Draw a bounding box around every parasitised red blood cell, every trophozoite, every gametocyte, every leukocyte, and every artifact (platelet-like body, stain precipitate, or debris).
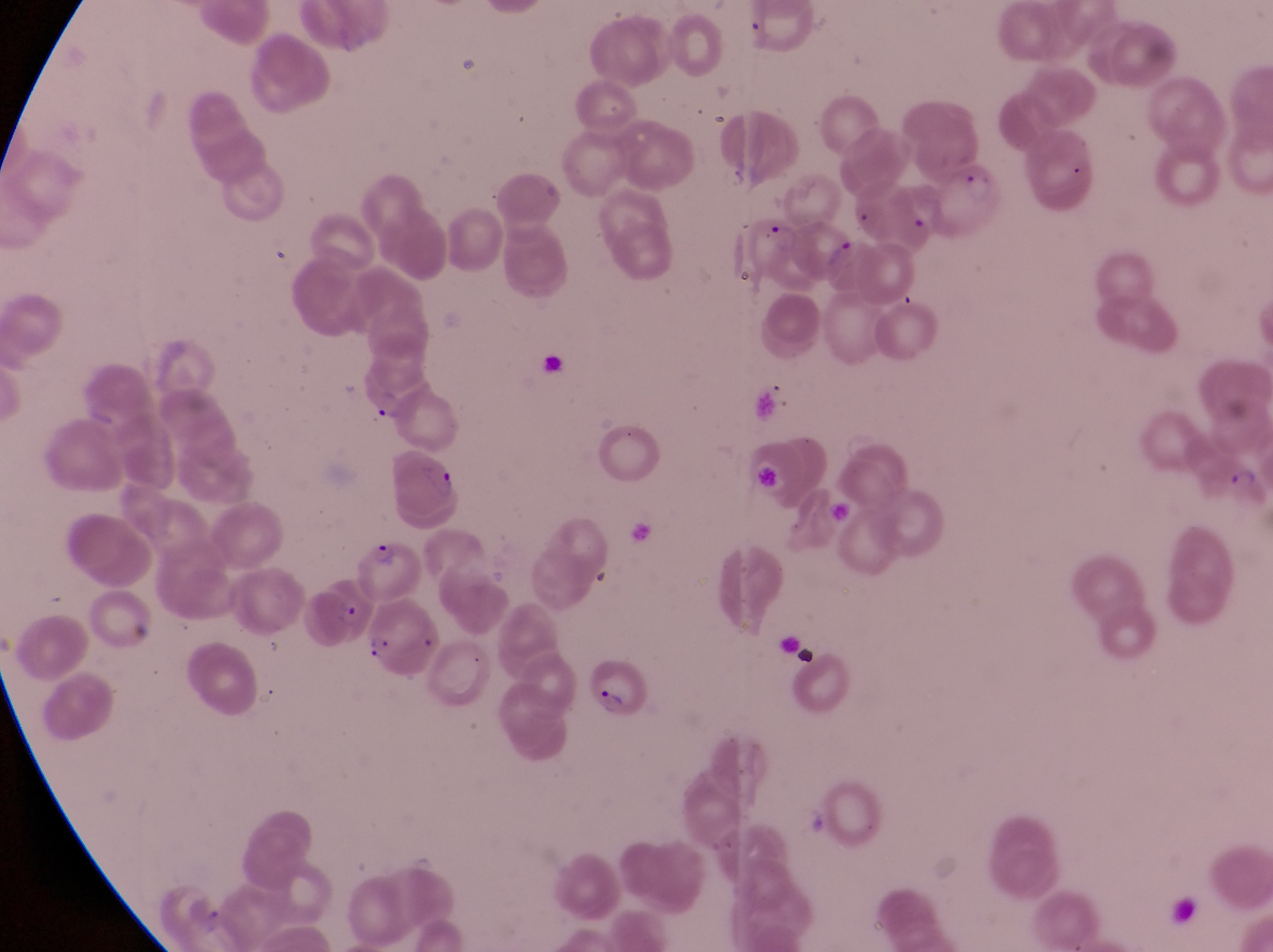
Approximate bounding boxes as {left, top, right, bottom} in pixels.
Parasitised red blood cells: {938, 164, 1010, 236}, {734, 212, 808, 295}, {819, 234, 886, 302}, {391, 457, 469, 532}, {352, 537, 427, 594}, {315, 579, 384, 641}, {581, 652, 661, 724}.
No leukocytes observed.
Artifacts (platelet-like body, stain precipitate, or debris): {776, 635, 818, 667}.

capture = smartphone photograph through the eyepiece of an Olympus CX-23 microscope
image size = 1273×952 pixels
field of view = single
preparation = thin blood smear
magnification = 1000x
country = Uganda